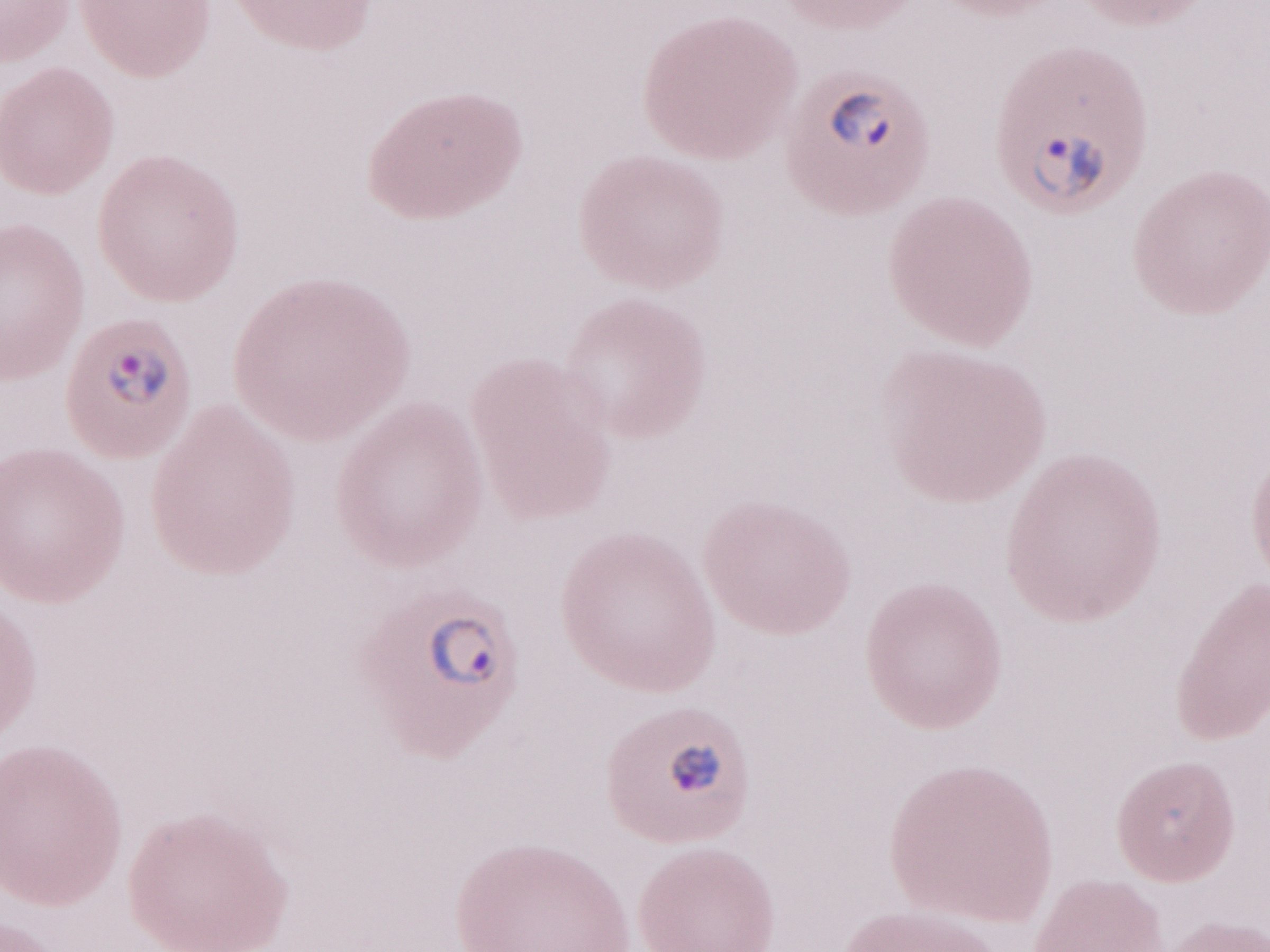
Image is 1270×952 pixels. Patient-level malaria diagnosis: positive. Olympus BX43 microscope, Olympus DP73 camera. One field of this slide. Magnification: 1,000x. Thin blood film. May-Grünwald-Giemsa stain.